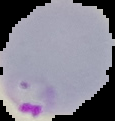

image type = segmented cell region on a black background
preparation = thin blood smear
result = Plasmodium parasites detected
image size = 115×121 pixels